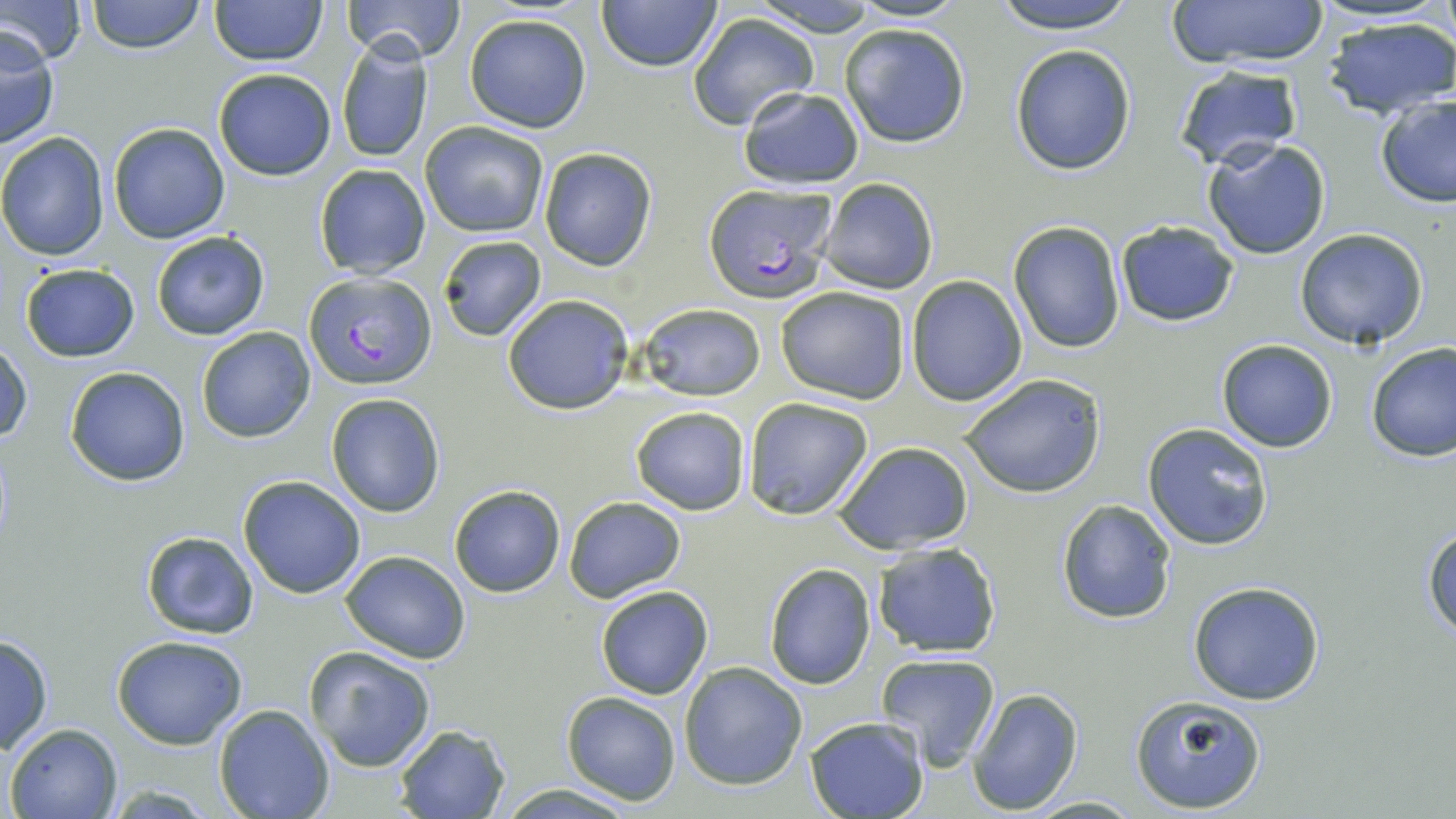

plasmodium_falciparum_infected_red_blood_cell_locations: 'approximate bounding boxes as (x1, y1, x2, y2) in pixels: (701, 185, 837, 301), (305, 271, 436, 389)'
slide_level_diagnosis: Plasmodium falciparum
magnification: 1000x
stain: May-Grünwald-Giemsa
modality: light microscopy
uninfected_red_blood_cell_locations: 'approximate bounding boxes as (x1, y1, x2, y2) in pixels: (0, 0, 85, 66), (85, 0, 205, 53), (208, 0, 326, 66), (343, 0, 466, 63), (595, 0, 725, 72), (748, 0, 885, 38), (849, 0, 964, 23), (989, 0, 1140, 35), (1168, 0, 1329, 68), (687, 11, 819, 129), (464, 13, 592, 134), (1322, 15, 1456, 120), (839, 22, 972, 148), (0, 27, 60, 148), (335, 37, 435, 165), (1009, 44, 1137, 176), (1172, 64, 1304, 170), (212, 68, 336, 180), (738, 87, 864, 191), (1374, 94, 1456, 208), (420, 121, 549, 237), (107, 122, 231, 244), (0, 132, 111, 260), (1202, 139, 1332, 260), (538, 147, 658, 271), (313, 164, 431, 279), (817, 178, 940, 295), (1113, 220, 1240, 328), (1006, 221, 1126, 353), (151, 230, 272, 341), (1293, 230, 1431, 351), (436, 235, 547, 342), (17, 261, 142, 363), (906, 275, 1027, 407), (775, 286, 912, 404), (502, 294, 631, 415), (637, 303, 767, 400), (195, 326, 316, 444), (1216, 339, 1338, 453), (1, 340, 32, 447), (1366, 342, 1456, 462), (65, 365, 190, 487), (960, 373, 1107, 499), (325, 392, 447, 517), (742, 396, 874, 521), (629, 406, 751, 514), (1142, 421, 1275, 552), (832, 440, 974, 555), (237, 475, 366, 597), (448, 484, 565, 597), (563, 495, 685, 602), (1056, 498, 1179, 624), (1423, 525, 1456, 639), (140, 530, 262, 640), (870, 541, 1003, 657), (339, 550, 471, 664), (764, 564, 877, 690), (1188, 580, 1325, 705), (594, 585, 713, 700), (0, 631, 54, 757), (111, 636, 249, 750), (304, 646, 436, 772), (876, 652, 1001, 770), (679, 661, 807, 790), (966, 687, 1084, 815), (560, 691, 681, 806), (1128, 691, 1269, 813), (214, 705, 336, 819), (803, 716, 929, 819), (5, 723, 122, 818), (392, 723, 511, 818), (494, 784, 643, 817), (1022, 795, 1147, 817)'
field_of_view: single
image_size: 1456×819 pixels
preparation: thin blood smear